State which parasite is depicted.
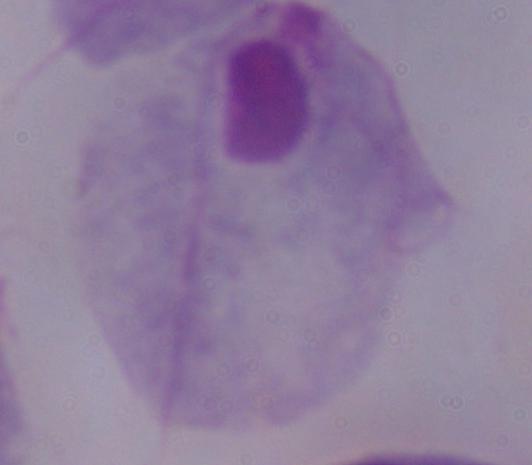

A trichomonad.

Summary:
  - Modality: micrograph
  - Magnification: 1000x